Assess this cell for malaria.
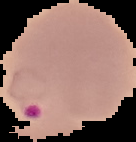
Parasitized.

Summary:
  - Image size: 136×142 pixels
  - Preparation: thin blood film
  - Image type: segmented cell region with the area outside set to black